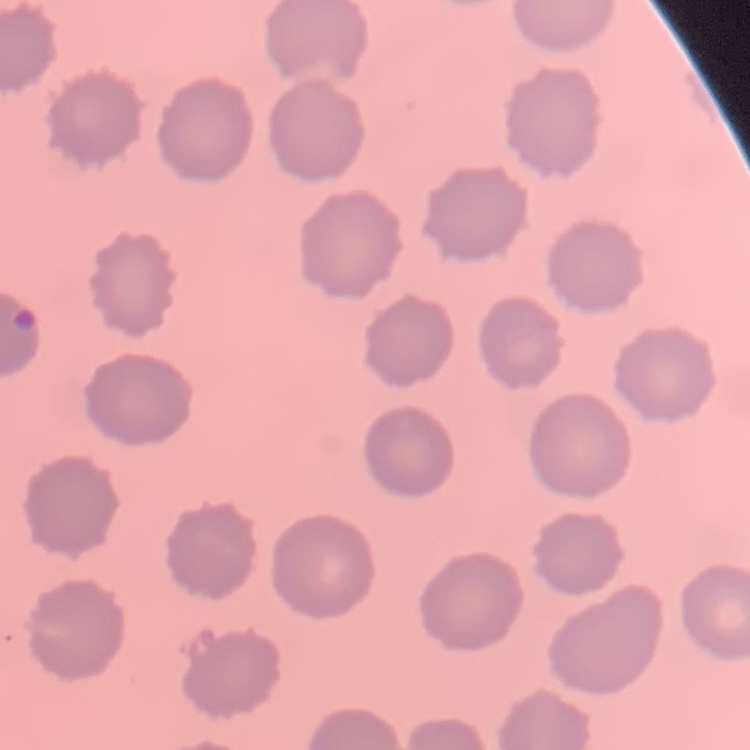 The erythrocytes exhibit no rouleaux formation. One tile cut from a larger photomicrograph. Thin peripheral smear. Field's or Giemsa stain.